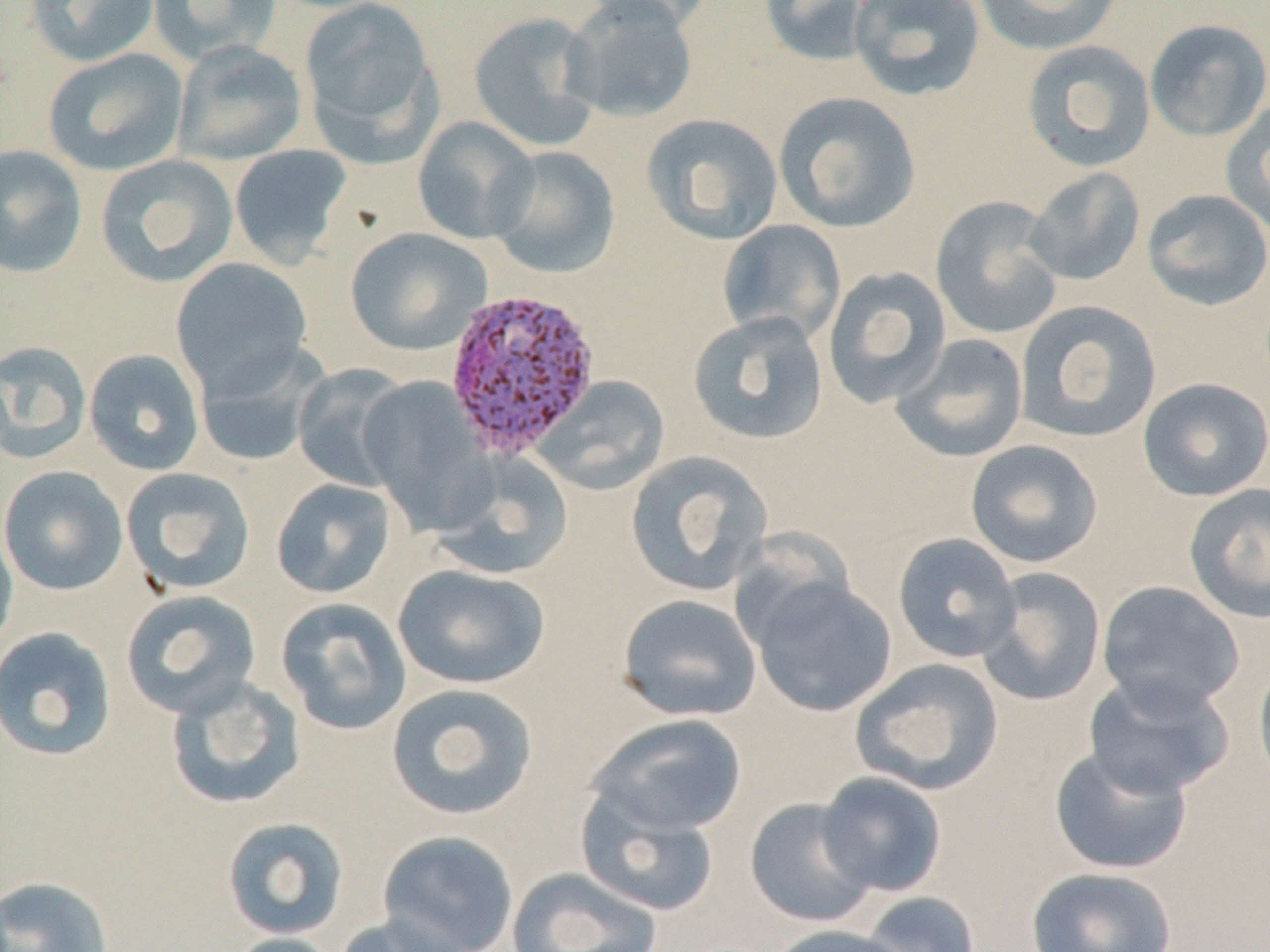

Summary:
  - Coordinate format: approximate bounding boxes as (x1, y1, x2, y2) in pixels
  - Uninfected red blood cell locations: (26, 0, 160, 67), (148, 0, 282, 64), (298, 0, 441, 152), (578, 0, 717, 32), (758, 0, 877, 66), (848, 0, 986, 102), (973, 0, 1123, 55), (560, 1, 700, 124), (468, 11, 603, 151), (1145, 18, 1270, 142), (172, 39, 307, 167), (1021, 40, 1156, 173), (43, 48, 189, 177), (773, 91, 921, 233), (1221, 99, 1270, 237), (640, 113, 783, 245), (412, 116, 540, 244), (0, 144, 87, 279), (229, 145, 353, 270), (486, 145, 621, 279), (95, 154, 239, 287), (1024, 167, 1146, 286), (1141, 189, 1270, 311), (931, 196, 1064, 340), (716, 219, 846, 345), (345, 227, 492, 356), (170, 257, 313, 396), (822, 266, 952, 408), (1015, 300, 1162, 443), (687, 311, 829, 445), (891, 333, 1029, 463), (0, 340, 91, 464), (194, 341, 331, 466), (84, 349, 205, 476), (293, 364, 411, 491), (358, 375, 493, 531), (534, 376, 670, 494), (1137, 377, 1270, 501), (966, 440, 1104, 568), (431, 451, 574, 580), (625, 451, 774, 597), (0, 465, 128, 596), (120, 467, 256, 595), (271, 478, 396, 599), (1183, 483, 1270, 624), (0, 518, 19, 655), (892, 533, 1022, 663), (393, 564, 550, 689), (975, 567, 1107, 707), (744, 572, 897, 717), (1097, 580, 1245, 714), (120, 589, 262, 719), (617, 593, 763, 722), (275, 597, 412, 735), (0, 627, 117, 762), (1254, 657, 1270, 792), (851, 658, 1004, 795), (1083, 671, 1236, 798), (165, 675, 306, 810), (385, 683, 539, 821), (587, 713, 747, 837), (1048, 744, 1194, 875), (816, 771, 947, 897), (576, 786, 721, 917), (745, 797, 879, 928), (221, 817, 350, 941), (378, 830, 519, 952), (507, 866, 663, 952), (1026, 866, 1177, 952), (0, 875, 113, 952), (859, 891, 981, 952), (334, 916, 468, 952), (767, 924, 907, 952), (221, 933, 343, 952)
  - Plasmodium vivax-infected red blood cell locations: (442, 287, 601, 460)
  - Slide-level diagnosis: Plasmodium vivax
  - Image size: 1270×952 pixels
  - Field of view: one of a larger specimen
  - Stain: May-Grünwald-Giemsa
  - Magnification: 1000x
  - Preparation: thin blood smear
  - Modality: optical microscopy